Report the malaria status of this cell.
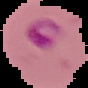

Parasitized.

The area outside the segmented cell region is set to black. Image is 88×88 pixels. From a thin blood smear.